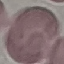

malaria status = uninfected
capture = smartphone through the microscope eyepiece
stain = Giemsa
preparation = thin blood film
image type = cell patch, automatically extracted from a larger field of view and resized to 64 × 64 pixels